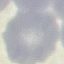
Summary:
  - Malaria status: uninfected
  - Image type: cell patch, automatically extracted from a larger field of view and resized to 64 × 64 pixels
  - Stain: Giemsa
  - Capture: smartphone through the microscope eyepiece
  - Preparation: thin blood smear